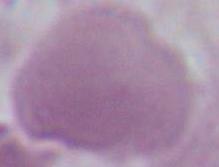
Summary:
  - Identification: red blood cell
  - Magnification: 1000x
  - Modality: micrograph